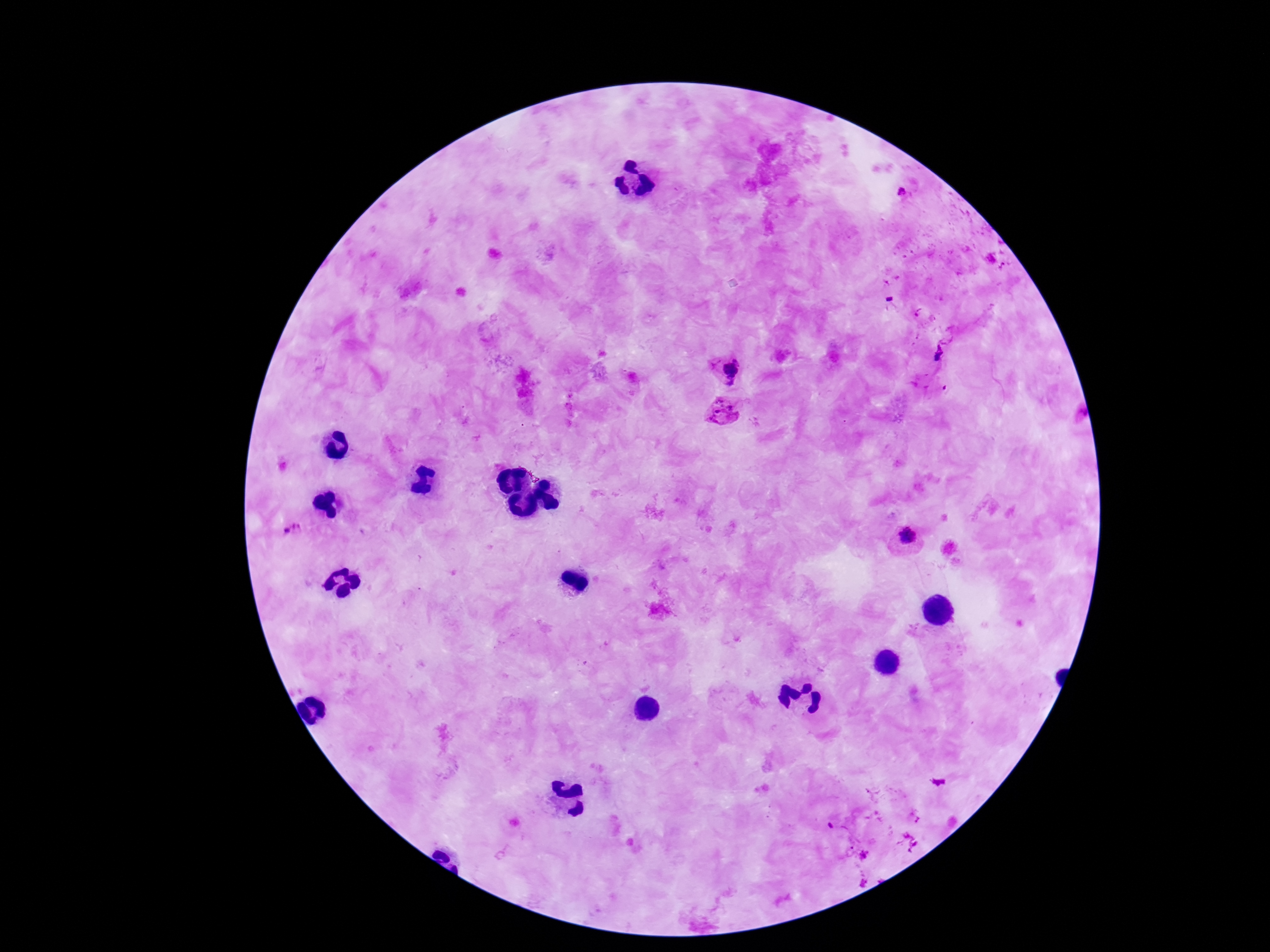

Approximate centers as (x, y) in pixels. Plasmodium parasite locations: (901, 194), (939, 353), (728, 370), (724, 412), (294, 530), (907, 535), (830, 826), (850, 852), (864, 855), (865, 881). 100x magnification. Patient malaria status: infected. Image is 1270×952 pixels. One field from this slide. Thick blood film. Giemsa stain. Photographed through the microscope eyepiece with a smartphone camera.